Comment on the background quality.
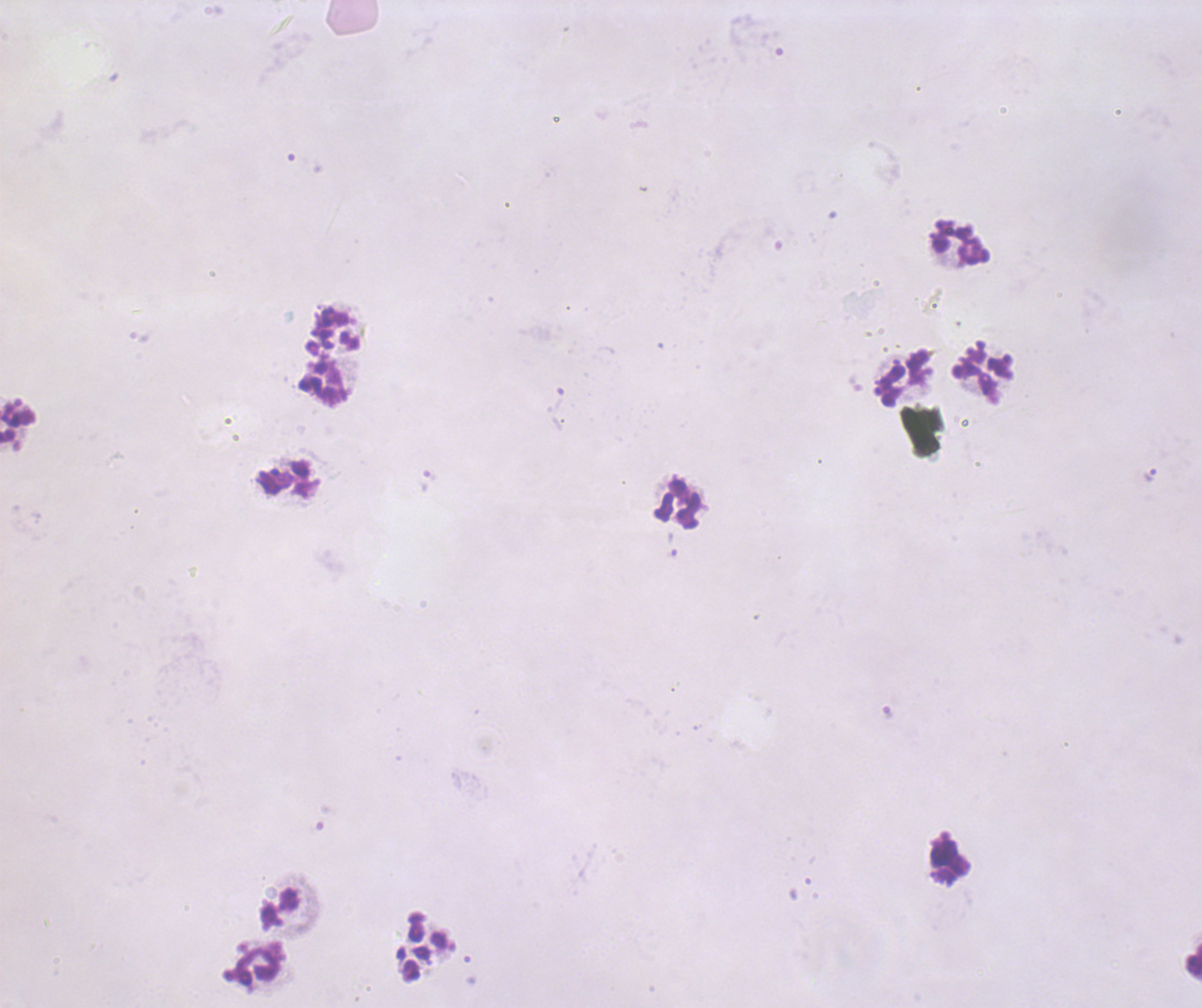

Poor.

Approximate centers as [x, y] in pixels.
Summary:
  - Trophozoite locations: [1150, 474]
  - Leukocyte locations: [960, 243], [982, 375], [902, 378], [322, 381], [288, 480], [677, 505], [948, 859], [278, 907], [1193, 962], [258, 966]
  - Context: previously used in a real diagnosis
  - Image size: 1202×1008 pixels
  - Coloration quality: bad
  - Magnification: 100x
  - Field of view: single
  - Stain: Romanowsky
  - Result: positive for malaria parasites
  - Preparation: thick blood smear